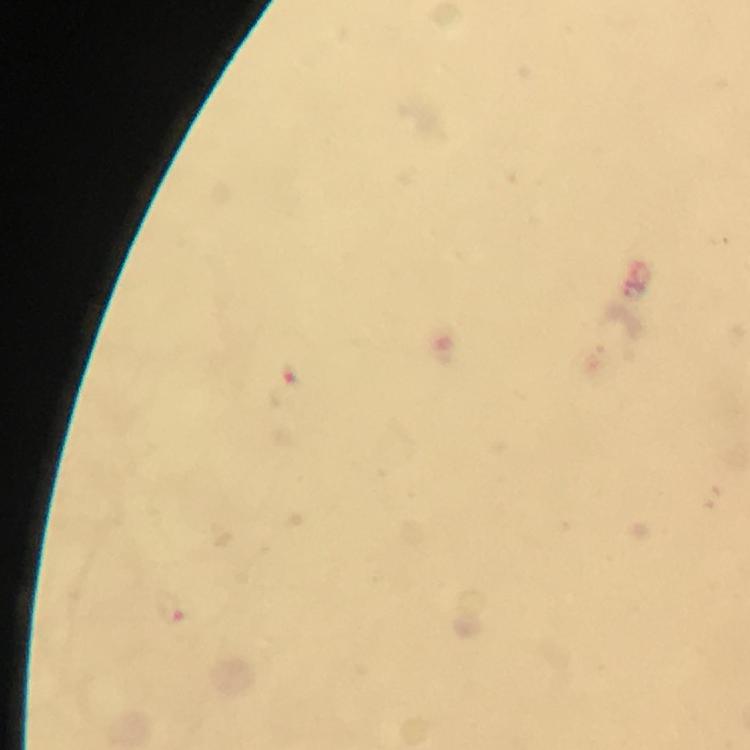
Approximate centers as (x, y) in pixels. Malaria parasite locations: (283, 390), (174, 612). Smartphone photograph taken through a microscope. A crop from one field of view. Giemsa-stained preparation. At 100x magnification. Immersion oil applied. Thick smear. From a diagnostic examination for malaria. Image is 750×750 pixels.